Identify the parasite.
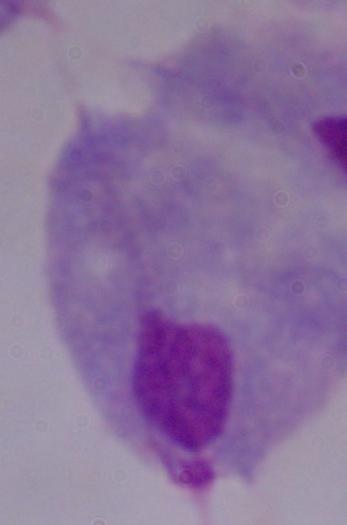

A trichomonad.

Summary:
  - Modality: micrograph
  - Magnification: 1000x